Point out each leukocyte.
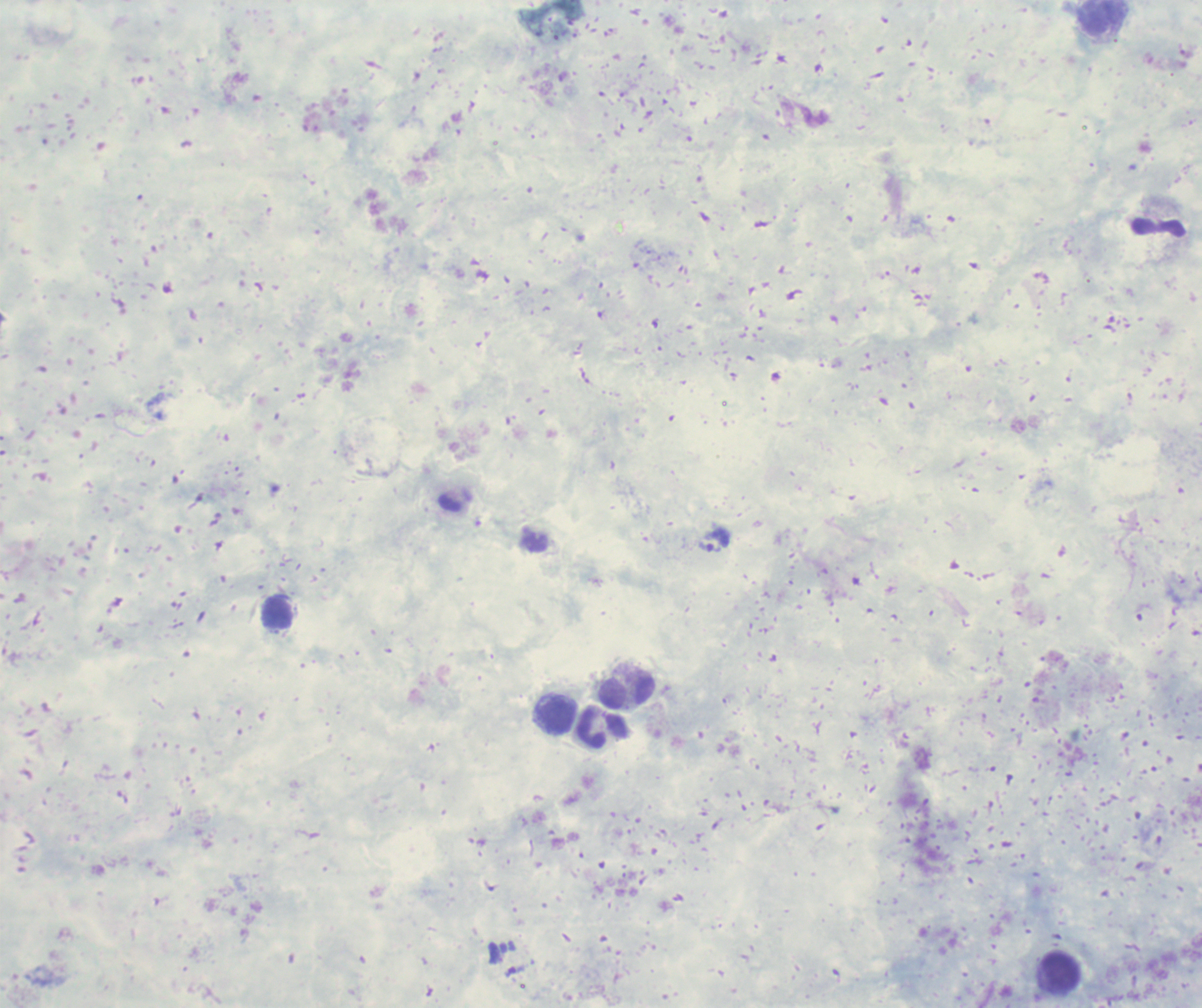
Approximate centers as (x, y) in pixels.
Leukocytes: (1104, 18), (1157, 228), (277, 612), (626, 690), (557, 714), (602, 727), (1060, 972).

Approximate centers as (x, y) in pixels. Trophozoite locations: (715, 539). Background quality: poor. Result: malaria parasites detected. Image is 1202×1008 pixels. Previously used in a real diagnosis. Single field of view. Captured at 100x magnification. Romanowsky-stained preparation. Thick smear of blood.